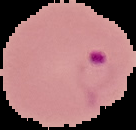
From a thin blood smear. Image is 136×130 pixels. Cell region segmented out of the field of view; the surrounding area is masked to black. Malaria status: parasitized.